Classify this cell by malaria status.
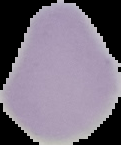
It is uninfected.

Summary:
  - Image type: segmented cell region with the area outside set to black
  - Preparation: thin blood film
  - Image size: 121×145 pixels